Evaluate for malaria.
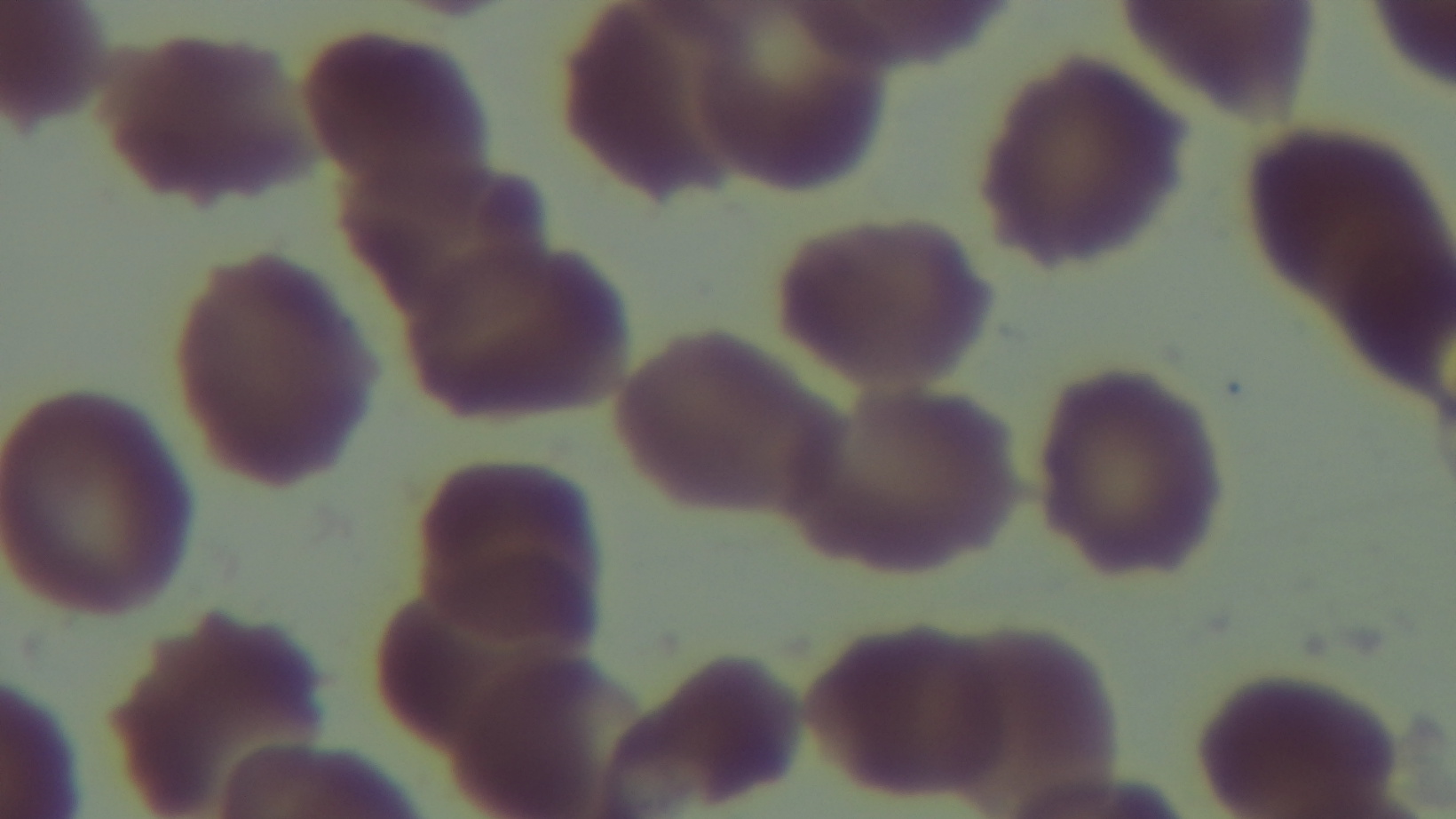
It is uninfected.

capture = mounted 4K digital camera
objective = 100x oil immersion
stain = Giemsa
modality = light microscopy
field of view = one from the slide
preparation = thin